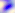

modality = micrograph
identification = Toxoplasma gondii
magnification = 400x